Point out each Plasmodium parasite.
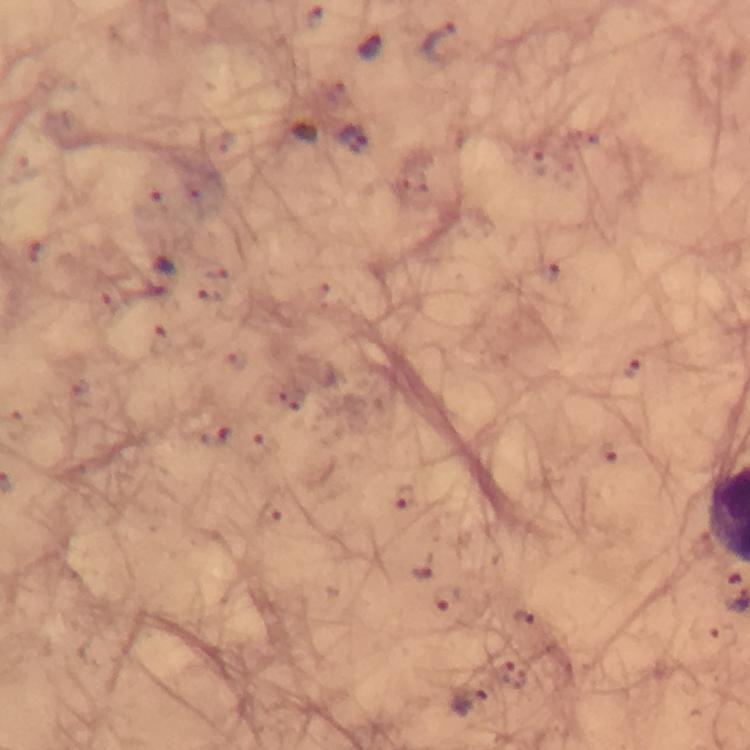
Approximate centers as (x, y) in pixels.
Plasmodium parasites: (442, 41), (370, 49), (354, 141), (36, 252), (158, 276), (632, 368), (215, 436), (609, 455), (404, 498), (422, 572), (448, 598), (524, 620), (470, 703).

Cropped region of a single field of view. Immersion oil applied. From a diagnostic examination for malaria. Smartphone photograph taken through a microscope. Image is 750×750 pixels. Giemsa-stained preparation. Thick blood smear. 100x magnification.